Name the parasite shown.
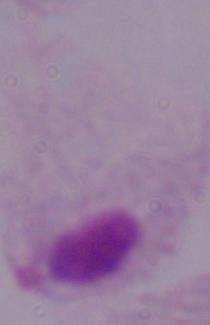
This is a trichomonad.

1000x magnification. Photomicrograph.